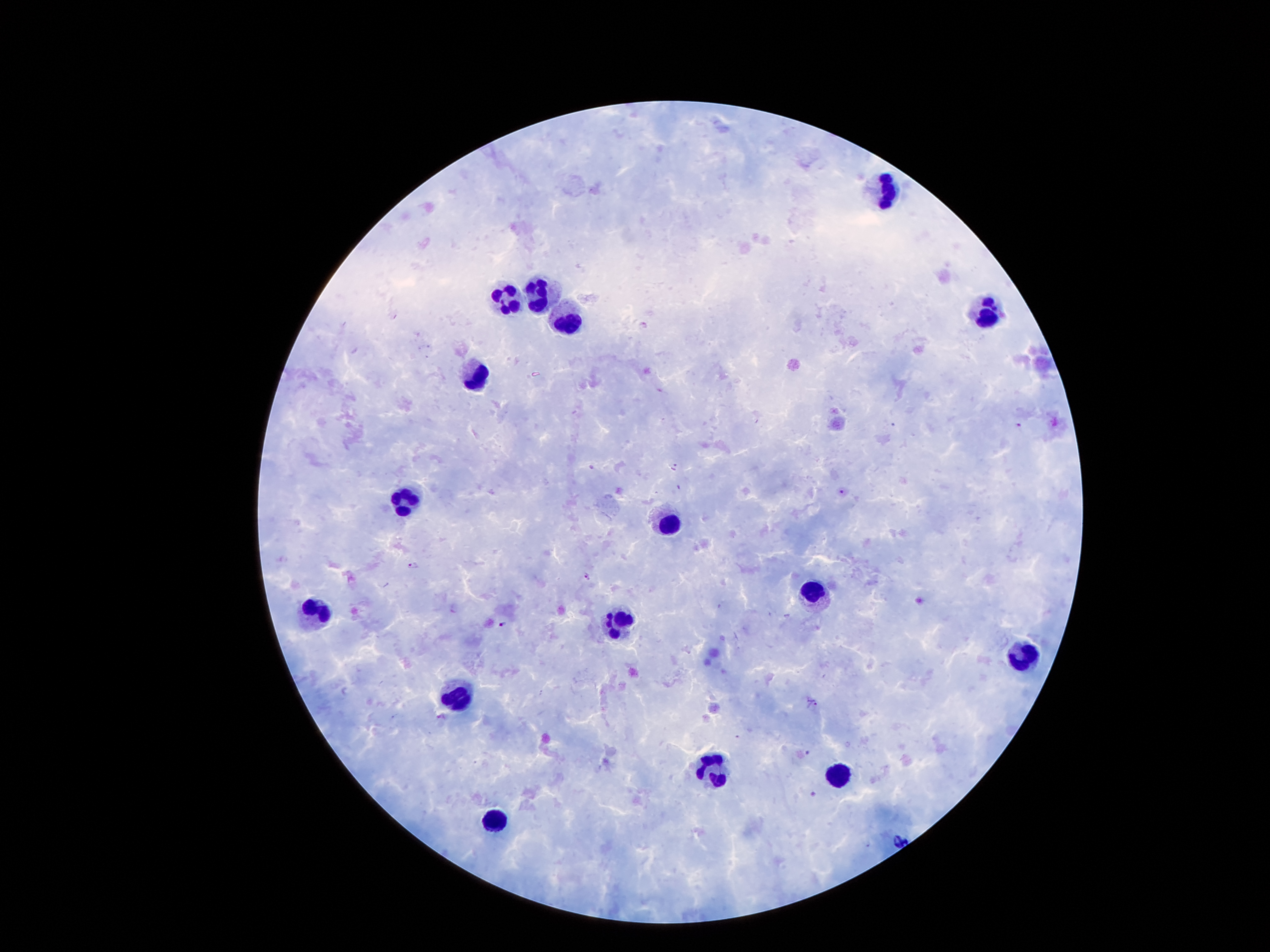

{
  "image_size": "1270×952 pixels",
  "patient_malaria_status": "infected with Plasmodium falciparum",
  "preparation": "thick blood smear",
  "magnification": "100x",
  "malaria_parasite_locations": "approximate object centers, in pixels from the top-left corner: (x=643, y=328), (x=1019, y=425), (x=591, y=467), (x=675, y=467), (x=841, y=492), (x=412, y=566), (x=587, y=576), (x=503, y=623), (x=813, y=702), (x=738, y=736), (x=807, y=752), (x=812, y=793)",
  "leukocyte_locations": "approximate object centers, in pixels from the top-left corner: (x=882, y=189), (x=538, y=294), (x=501, y=300), (x=983, y=313), (x=566, y=319), (x=473, y=374), (x=403, y=500), (x=669, y=520), (x=812, y=591), (x=314, y=610), (x=611, y=624), (x=1025, y=651), (x=456, y=700), (x=711, y=770), (x=837, y=775), (x=496, y=820)",
  "stain": "Giemsa",
  "field_of_view": "single",
  "capture": "smartphone camera through the microscope eyepiece"
}